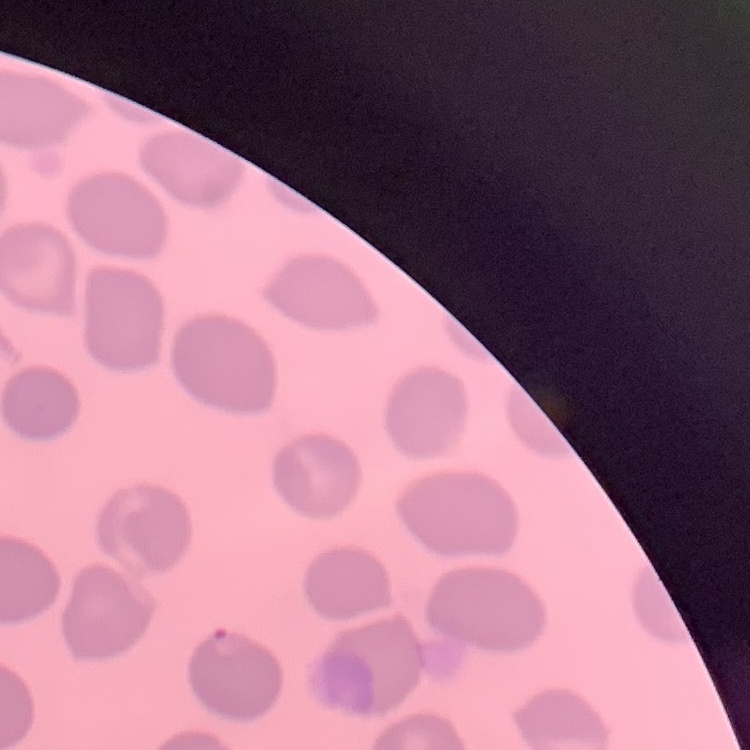
Summary:
  - Red blood cell morphology: no rouleaux formation
  - Stain: Field's or Giemsa
  - Image type: square crop of a larger photomicrograph
  - Preparation: thin peripheral smear